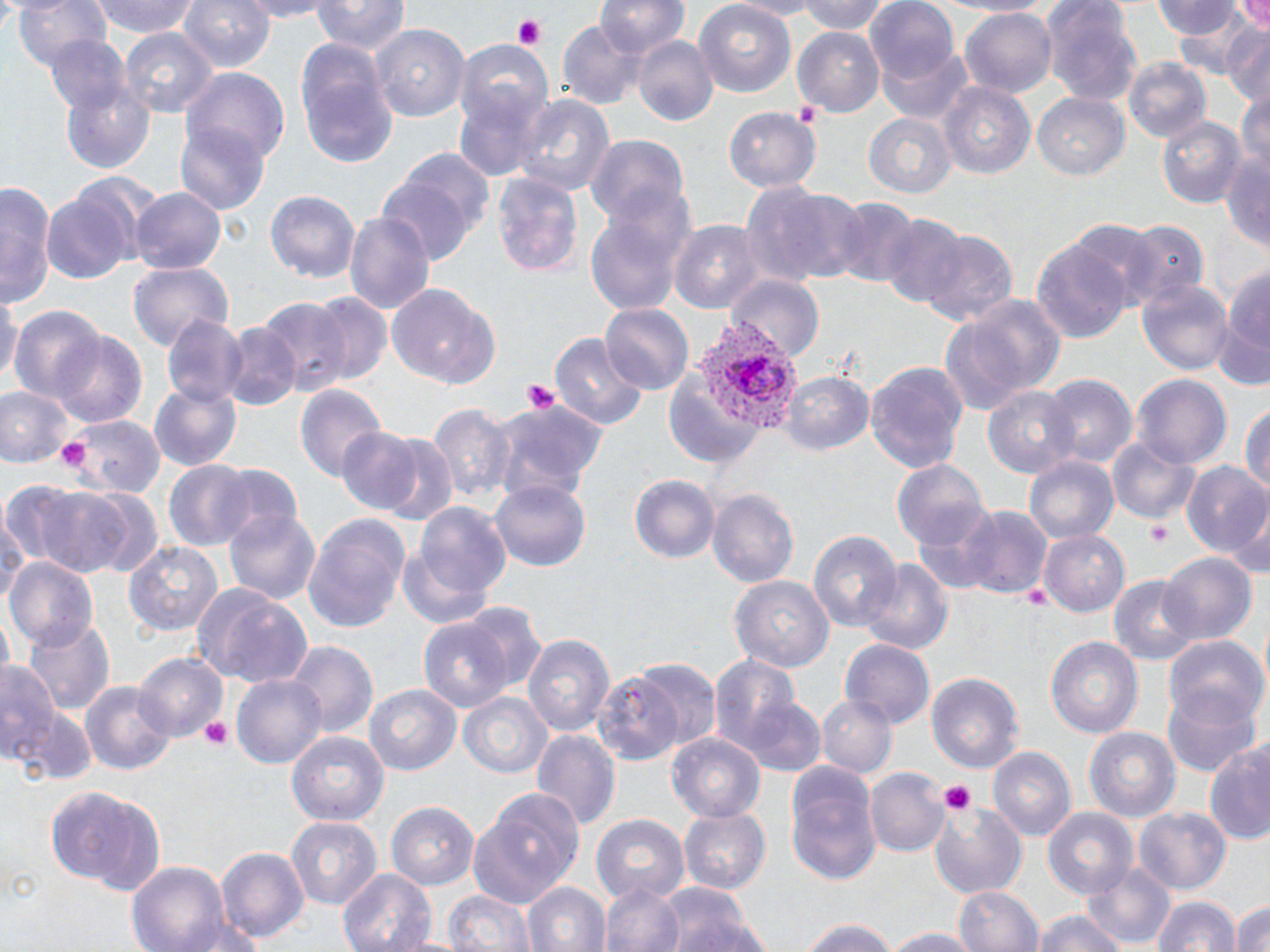
Approximate bounding boxes as [x1, y1, x2, y2] in pixels. Uninfected red blood cell locations: [5, 0, 113, 73], [92, 0, 200, 39], [179, 0, 278, 75], [235, 0, 346, 21], [313, 0, 407, 54], [596, 0, 690, 58], [727, 0, 822, 18], [798, 0, 891, 35], [1043, 0, 1141, 105], [865, 1, 964, 88], [1152, 1, 1244, 45], [1229, 1, 1270, 37], [692, 4, 797, 97], [960, 7, 1057, 98], [556, 18, 650, 110], [1223, 23, 1270, 109], [372, 25, 469, 124], [792, 26, 886, 116], [121, 29, 216, 122], [44, 35, 135, 119], [633, 37, 718, 124], [293, 39, 396, 170], [882, 44, 977, 125], [454, 49, 553, 179], [1121, 59, 1213, 147], [59, 69, 157, 179], [182, 70, 290, 169], [936, 81, 1036, 180], [1235, 82, 1270, 177], [511, 91, 616, 197], [1032, 93, 1130, 182], [725, 106, 819, 190], [864, 111, 959, 195], [1155, 114, 1247, 209], [176, 120, 270, 216], [585, 138, 690, 232], [1220, 149, 1270, 253], [380, 155, 490, 264], [491, 171, 586, 279], [2, 182, 58, 307], [744, 184, 866, 288], [131, 187, 226, 275], [42, 189, 134, 285], [263, 189, 357, 283], [834, 199, 921, 288], [583, 209, 687, 314], [345, 210, 434, 317], [877, 210, 965, 307], [669, 221, 760, 311], [1125, 222, 1209, 307], [918, 230, 1016, 327], [1032, 239, 1132, 345], [1220, 256, 1270, 383], [127, 262, 233, 353], [726, 273, 823, 359], [1139, 278, 1233, 377], [385, 283, 501, 389], [0, 288, 20, 388], [303, 291, 392, 388], [947, 292, 1069, 413], [260, 298, 348, 394], [600, 303, 692, 391], [9, 307, 105, 406], [163, 314, 249, 409], [221, 323, 301, 411], [51, 331, 148, 429], [549, 331, 649, 430], [865, 360, 970, 473], [780, 372, 875, 455], [1040, 375, 1136, 472], [1134, 375, 1231, 471], [149, 381, 243, 469], [295, 383, 385, 482], [0, 385, 76, 467], [983, 387, 1077, 478], [491, 398, 610, 510], [1242, 402, 1270, 502], [427, 405, 517, 509], [60, 415, 165, 498], [335, 427, 429, 515], [374, 435, 459, 528], [1110, 436, 1201, 525], [1024, 454, 1119, 544], [892, 459, 989, 549], [210, 462, 300, 546], [165, 463, 253, 549], [1182, 463, 1270, 562], [628, 475, 720, 565], [489, 479, 593, 572], [24, 483, 134, 576], [75, 488, 164, 578], [707, 489, 800, 590], [934, 502, 1049, 597], [415, 503, 516, 604], [0, 506, 31, 605], [1228, 506, 1269, 584], [224, 508, 320, 606], [301, 514, 411, 631], [1040, 529, 1129, 615], [806, 531, 903, 636], [124, 541, 222, 637], [1159, 552, 1256, 645], [6, 557, 99, 645], [864, 560, 953, 656], [1110, 576, 1198, 665], [730, 577, 833, 673], [191, 581, 313, 690], [461, 600, 547, 695], [23, 614, 117, 716], [419, 619, 512, 710], [521, 634, 617, 739], [1164, 635, 1266, 728], [1045, 636, 1145, 739], [841, 641, 934, 727], [286, 642, 376, 739], [134, 652, 228, 742], [709, 656, 804, 757], [0, 657, 66, 772], [621, 659, 721, 751], [928, 671, 1025, 776], [595, 673, 685, 763], [231, 674, 326, 769], [78, 681, 176, 778], [363, 682, 461, 777], [1163, 688, 1260, 776], [457, 691, 552, 781], [9, 694, 97, 783], [816, 695, 896, 779], [741, 697, 828, 779], [1085, 727, 1181, 826], [287, 728, 390, 823], [531, 729, 620, 828], [667, 735, 764, 820], [1208, 740, 1270, 846], [990, 746, 1076, 841], [785, 760, 881, 885], [867, 770, 948, 857], [49, 784, 168, 893], [469, 791, 583, 905], [929, 797, 1027, 896], [387, 803, 481, 891], [1134, 806, 1230, 892], [1041, 807, 1140, 900], [676, 808, 770, 894], [591, 812, 689, 902], [286, 816, 384, 912], [218, 847, 308, 947], [126, 862, 230, 950], [1081, 862, 1173, 946], [338, 867, 436, 952], [521, 880, 608, 952], [657, 881, 759, 952], [599, 883, 687, 952], [953, 885, 1043, 952], [441, 888, 536, 952], [1148, 892, 1239, 952], [1232, 896, 1270, 952], [1034, 910, 1130, 952], [180, 915, 263, 952], [796, 917, 904, 952], [879, 927, 983, 952]. Plasmodium vivax-infected red blood cell locations: [677, 323, 806, 444]. Platelet locations: [509, 14, 549, 50], [794, 100, 825, 129], [521, 379, 565, 415], [1148, 519, 1172, 546], [1022, 583, 1052, 613], [196, 715, 236, 750], [938, 781, 976, 816]. Slide-level diagnosis: Plasmodium vivax. Thin blood film. Image is 1270×952 pixels. Light microscopy. Single field of view. 1000x magnification. May-Grünwald-Giemsa stain.